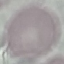

Summary:
  - Malaria status: uninfected
  - Capture: smartphone through the microscope eyepiece
  - Preparation: thin blood film
  - Stain: Giemsa
  - Image type: automatically extracted cell patch, resized to 64 × 64 pixels